Name the blood parasite species.
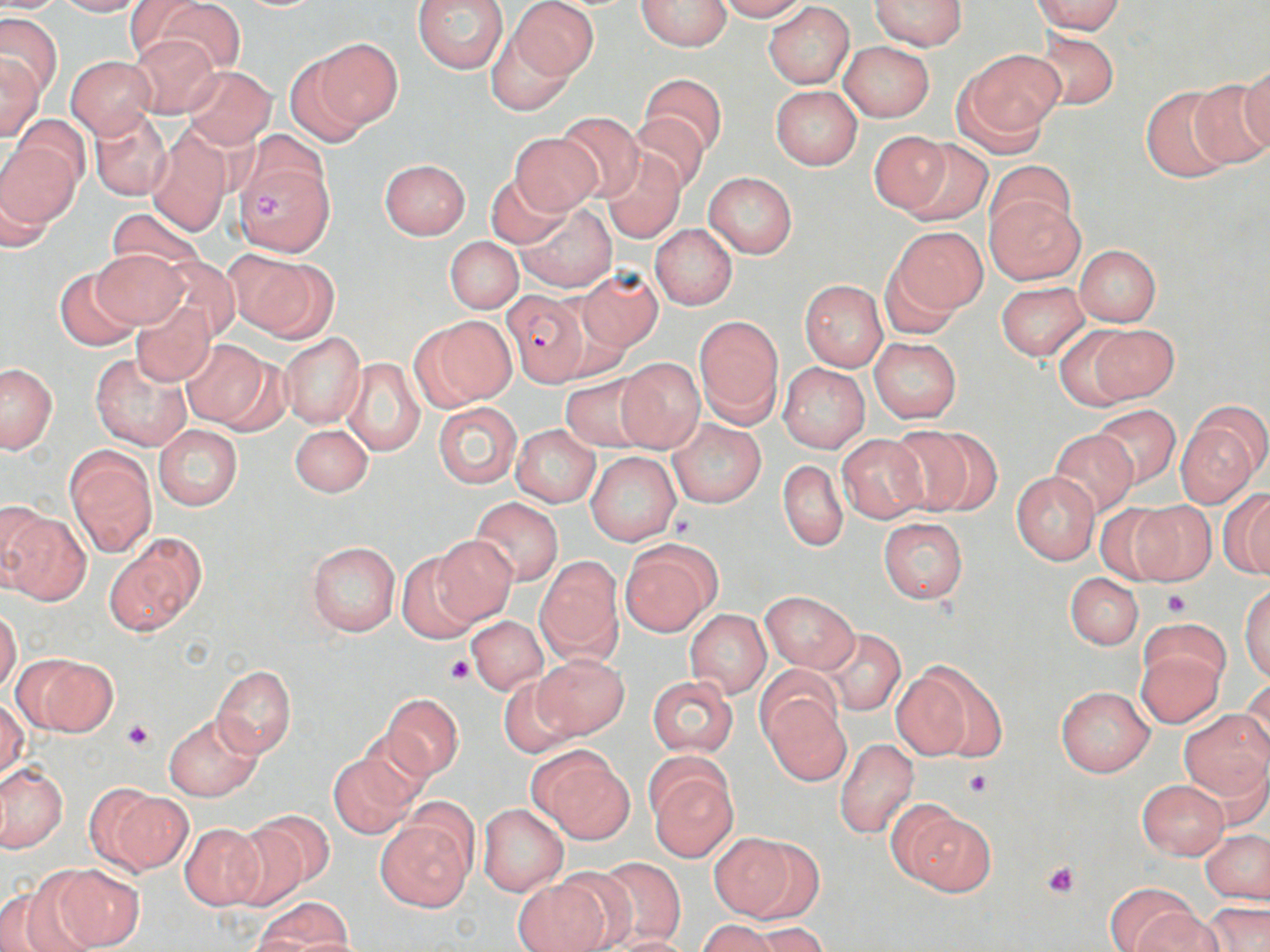

Plasmodium falciparum.

Approximate bounding boxes as (x1, y1, x2, y2) in pixels. Platelet locations: (253, 190, 285, 219), (1163, 590, 1193, 618), (445, 654, 477, 684), (122, 719, 155, 751), (964, 768, 996, 796), (1040, 861, 1081, 898). Plasmodium falciparum-infected red blood cell locations: (502, 291, 590, 386). Uninfected red blood cell locations: (0, 0, 66, 13), (52, 0, 149, 16), (139, 0, 246, 77), (413, 0, 510, 74), (509, 0, 597, 84), (635, 0, 732, 50), (714, 0, 808, 21), (1033, 0, 1124, 34), (869, 1, 967, 50), (763, 2, 855, 88), (0, 14, 62, 98), (485, 24, 577, 114), (1032, 30, 1120, 110), (127, 35, 222, 117), (311, 38, 403, 132), (839, 41, 934, 122), (958, 49, 1064, 145), (283, 51, 377, 145), (0, 55, 44, 141), (66, 55, 155, 136), (1238, 59, 1270, 157), (183, 65, 276, 149), (641, 72, 725, 158), (1190, 79, 1270, 171), (770, 85, 863, 169), (1139, 85, 1239, 183), (89, 109, 172, 201), (556, 112, 646, 202), (630, 112, 711, 194), (11, 113, 88, 193), (147, 128, 233, 234), (868, 131, 954, 214), (510, 132, 602, 214), (0, 136, 77, 238), (902, 139, 992, 226), (600, 150, 686, 243), (233, 156, 332, 256), (378, 159, 471, 239), (987, 159, 1074, 239), (704, 171, 798, 258), (485, 173, 571, 250), (984, 191, 1085, 284), (515, 202, 616, 291), (106, 207, 208, 276), (650, 224, 738, 310), (891, 227, 985, 319), (445, 237, 522, 314), (1074, 244, 1161, 326), (91, 249, 189, 328), (225, 250, 334, 340), (150, 256, 239, 344), (53, 268, 141, 350), (577, 270, 663, 351), (800, 280, 888, 372), (996, 282, 1090, 360), (129, 303, 216, 386), (694, 316, 784, 424), (418, 317, 515, 407), (1089, 324, 1177, 401), (1052, 325, 1146, 410), (279, 333, 366, 428), (869, 337, 962, 423), (180, 338, 278, 431), (91, 352, 192, 451), (340, 358, 426, 455), (615, 358, 705, 453), (777, 361, 870, 454), (0, 363, 56, 453), (559, 373, 653, 453), (433, 402, 521, 487), (1091, 405, 1181, 487), (667, 419, 766, 509), (1177, 421, 1259, 508), (290, 422, 373, 498), (154, 424, 242, 511), (512, 424, 600, 507), (885, 424, 996, 519), (1048, 429, 1139, 519), (836, 434, 930, 523), (64, 446, 158, 556), (585, 451, 682, 547), (778, 461, 847, 551), (1010, 470, 1100, 565), (1218, 491, 1270, 578), (469, 497, 565, 586), (0, 498, 48, 588), (1129, 500, 1217, 585), (1092, 502, 1181, 584), (1, 504, 87, 604), (878, 518, 967, 604), (430, 534, 516, 625), (106, 537, 204, 635), (619, 540, 720, 637), (306, 541, 400, 637), (395, 554, 484, 643), (535, 556, 623, 663), (1065, 571, 1143, 650), (1240, 583, 1270, 682), (760, 591, 859, 672), (0, 608, 23, 694), (686, 610, 771, 698), (466, 616, 548, 694), (822, 628, 905, 715), (1135, 641, 1225, 728), (20, 653, 117, 737), (533, 654, 629, 739), (891, 660, 1004, 763), (211, 664, 297, 757), (757, 665, 842, 743), (497, 675, 579, 758), (646, 675, 739, 757), (1242, 679, 1270, 765), (1055, 685, 1154, 776), (380, 692, 464, 781), (762, 693, 850, 784), (0, 699, 27, 780), (1178, 709, 1270, 800), (163, 714, 261, 801), (834, 738, 919, 840), (528, 746, 631, 843), (328, 752, 420, 838), (0, 763, 67, 854), (647, 765, 738, 861), (1136, 779, 1230, 859), (97, 786, 191, 876), (477, 804, 567, 896), (893, 804, 996, 896), (247, 808, 337, 894), (374, 814, 473, 912), (221, 820, 311, 911), (180, 822, 265, 910), (1201, 829, 1270, 904), (708, 832, 810, 921), (596, 856, 685, 947), (42, 863, 144, 950), (550, 868, 638, 949), (510, 875, 611, 952), (0, 877, 96, 952), (1107, 883, 1198, 951), (258, 897, 353, 950), (1203, 901, 1270, 951), (1136, 908, 1223, 952), (697, 919, 783, 952), (750, 921, 827, 952), (606, 935, 694, 952). Captured at 1000x magnification. May-Grünwald-Giemsa stain. Thin blood film. Light microscopy. One field of a larger specimen. Image is 1270×952 pixels.